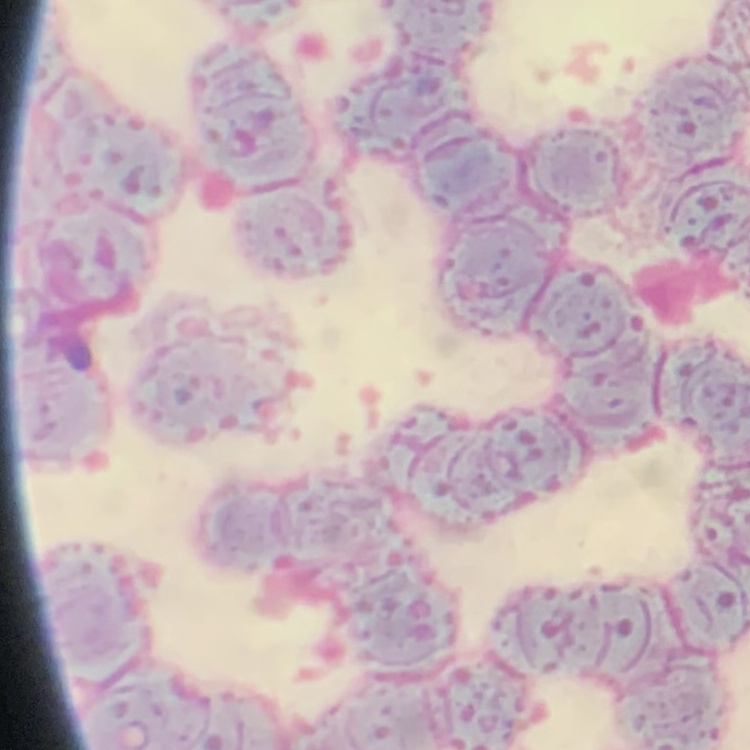

erythrocyte_morphology: rouleaux formation
preparation: thin blood film
image_type: one tile cut from a larger photomicrograph
stain: Field's or Giemsa